Give the position of every leukocyte visible.
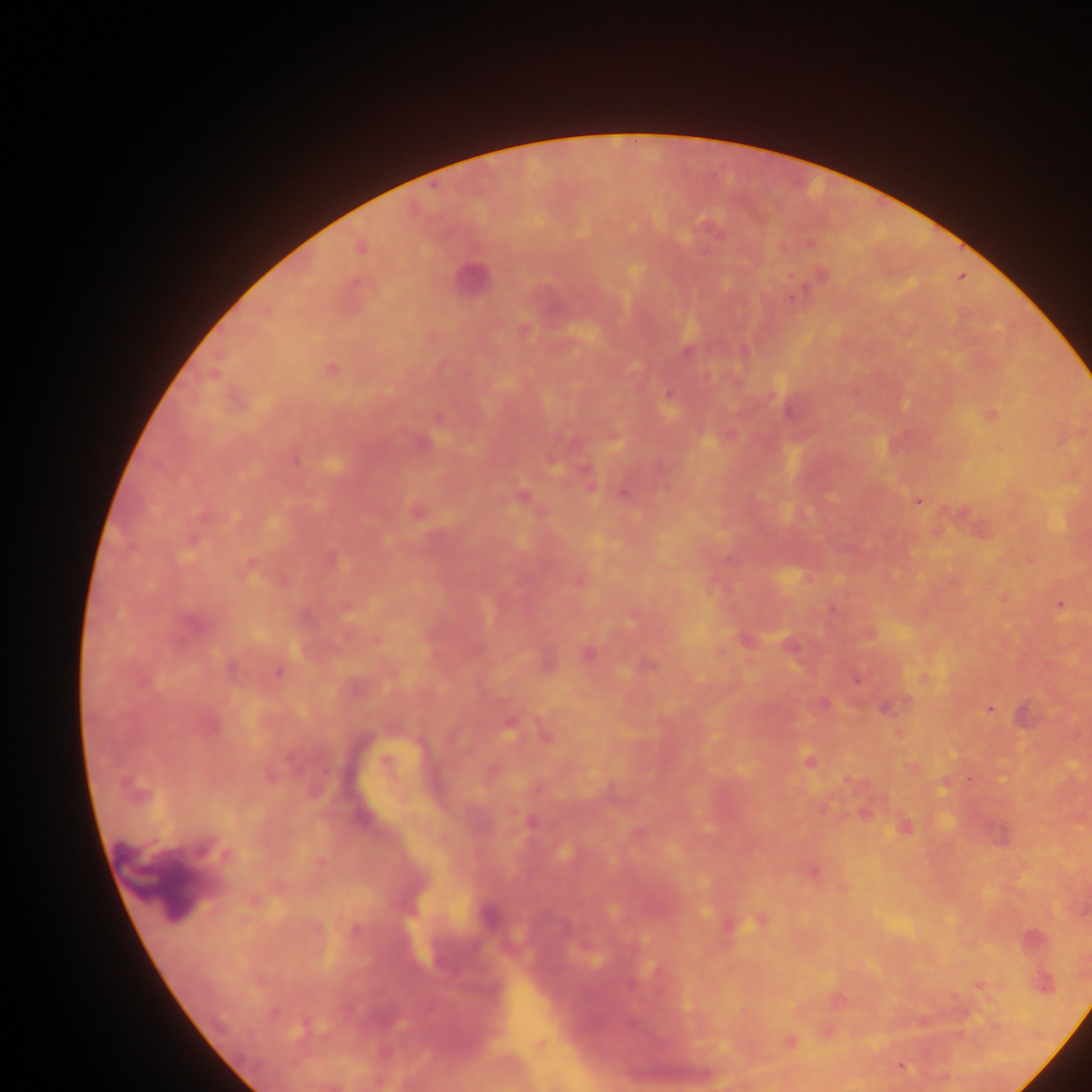
No leukocytes observed.

image size = 1092×1092 pixels
field of view = single
Plasmodium parasite locations = approximate centers as (x, y) in pixels: (809, 242), (791, 296), (667, 392), (990, 414), (295, 458), (589, 484), (622, 493), (918, 501), (415, 509), (1002, 597), (1060, 604), (279, 672), (855, 680), (990, 708), (981, 985), (900, 1067)
capture = mobile-phone photograph through a microscope
country = Ghana
preparation = thick blood film